Identify the cell.
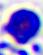

A leukocyte.

400x magnification. Micrograph.